Locate every blood parasite and identify its species.
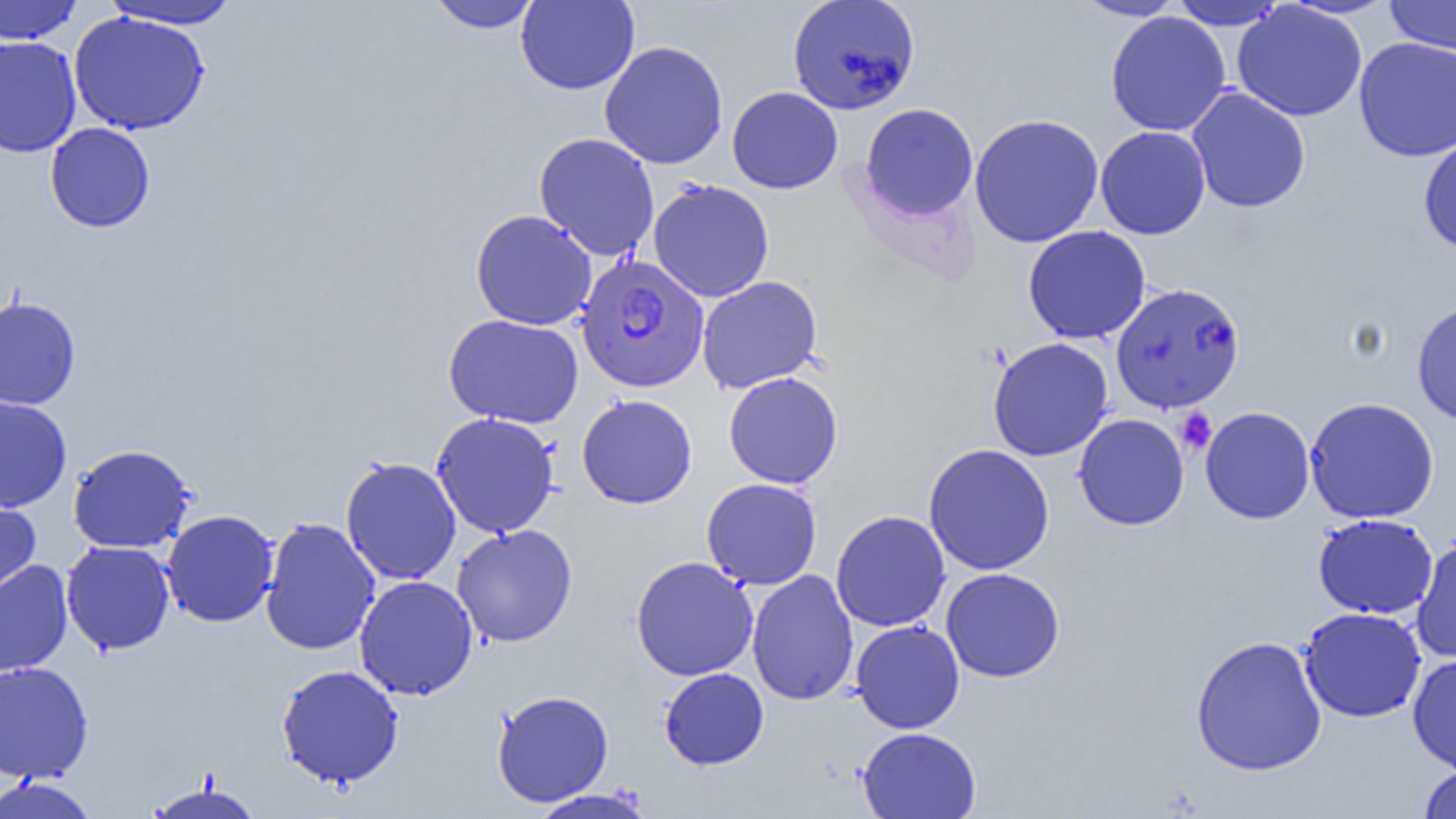

Approximate bounding boxes as [x1, y1, x2, y2] in pixels.
Plasmodium falciparum-infected red blood cells: [576, 255, 709, 392], [1111, 282, 1245, 414].
No Plasmodium ovale, Plasmodium malariae, Plasmodium vivax, Babesia divergens, or Trypanosoma brucei observed.

Summary:
  - Uninfected red blood cell locations: [0, 0, 83, 44], [101, 0, 242, 30], [426, 0, 542, 33], [515, 0, 640, 95], [787, 0, 920, 114], [1075, 0, 1187, 21], [1169, 1, 1286, 30], [1386, 1, 1456, 54], [1232, 2, 1367, 121], [69, 11, 210, 135], [1105, 11, 1232, 137], [0, 35, 82, 158], [1353, 36, 1456, 161], [599, 40, 728, 169], [727, 86, 843, 194], [1187, 87, 1311, 213], [860, 103, 979, 221], [969, 113, 1104, 248], [45, 122, 156, 232], [1096, 126, 1211, 239], [533, 132, 660, 261], [1418, 134, 1456, 255], [647, 178, 775, 303], [470, 209, 597, 330], [1022, 225, 1151, 344], [696, 276, 823, 393], [0, 295, 81, 410], [1411, 299, 1456, 426], [443, 313, 584, 428], [987, 337, 1114, 462], [723, 371, 843, 489], [576, 393, 698, 509], [0, 396, 72, 512], [1304, 396, 1440, 524], [1200, 406, 1316, 524], [430, 412, 560, 538], [1073, 414, 1189, 530], [923, 443, 1055, 575], [68, 444, 197, 553], [340, 456, 461, 585], [701, 478, 823, 590], [0, 495, 41, 606], [160, 510, 279, 627], [830, 510, 951, 632], [1313, 513, 1438, 619], [259, 517, 381, 656], [451, 524, 578, 647], [1411, 536, 1456, 664], [61, 540, 175, 655], [630, 556, 758, 681], [0, 559, 74, 677], [941, 567, 1065, 683], [746, 570, 859, 706], [354, 575, 478, 700], [1299, 607, 1426, 723], [850, 620, 965, 734], [1189, 634, 1328, 776], [1407, 653, 1456, 775], [0, 661, 94, 784], [275, 664, 405, 788], [659, 668, 768, 770], [491, 690, 614, 807], [857, 727, 981, 818], [1418, 764, 1456, 819], [0, 776, 100, 819], [144, 780, 264, 819], [526, 787, 658, 819]
  - Platelet locations: [1175, 407, 1216, 455]
  - Slide-level diagnosis: Plasmodium falciparum
  - Image size: 1456×819 pixels
  - Magnification: 1000x
  - Preparation: thin blood film
  - Modality: light microscopy
  - Field of view: one of a larger specimen